Comment on the morphology of the erythrocytes.
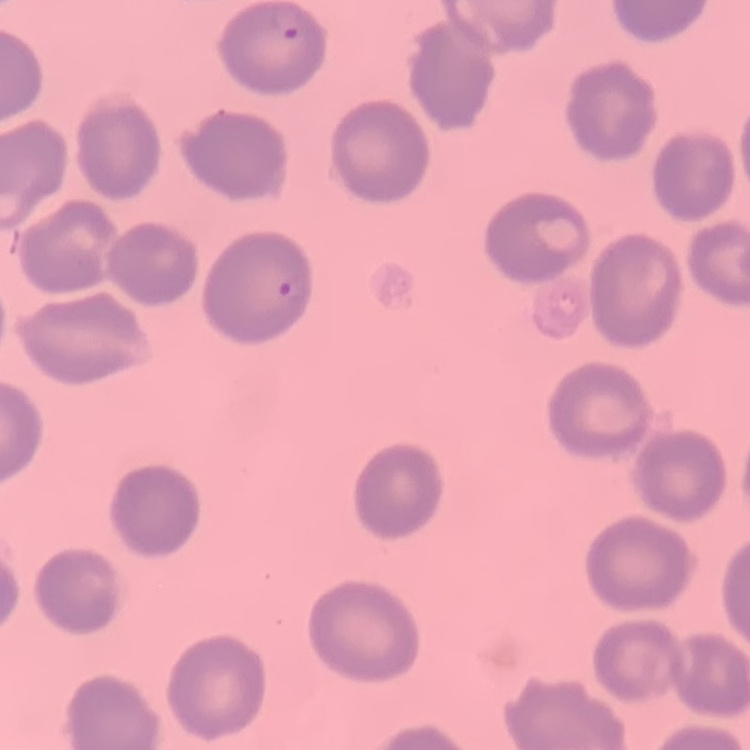

No rouleaux formation.

Summary:
  - Image type: square crop of a larger photomicrograph
  - Stain: Field's or Giemsa
  - Preparation: thin peripheral smear